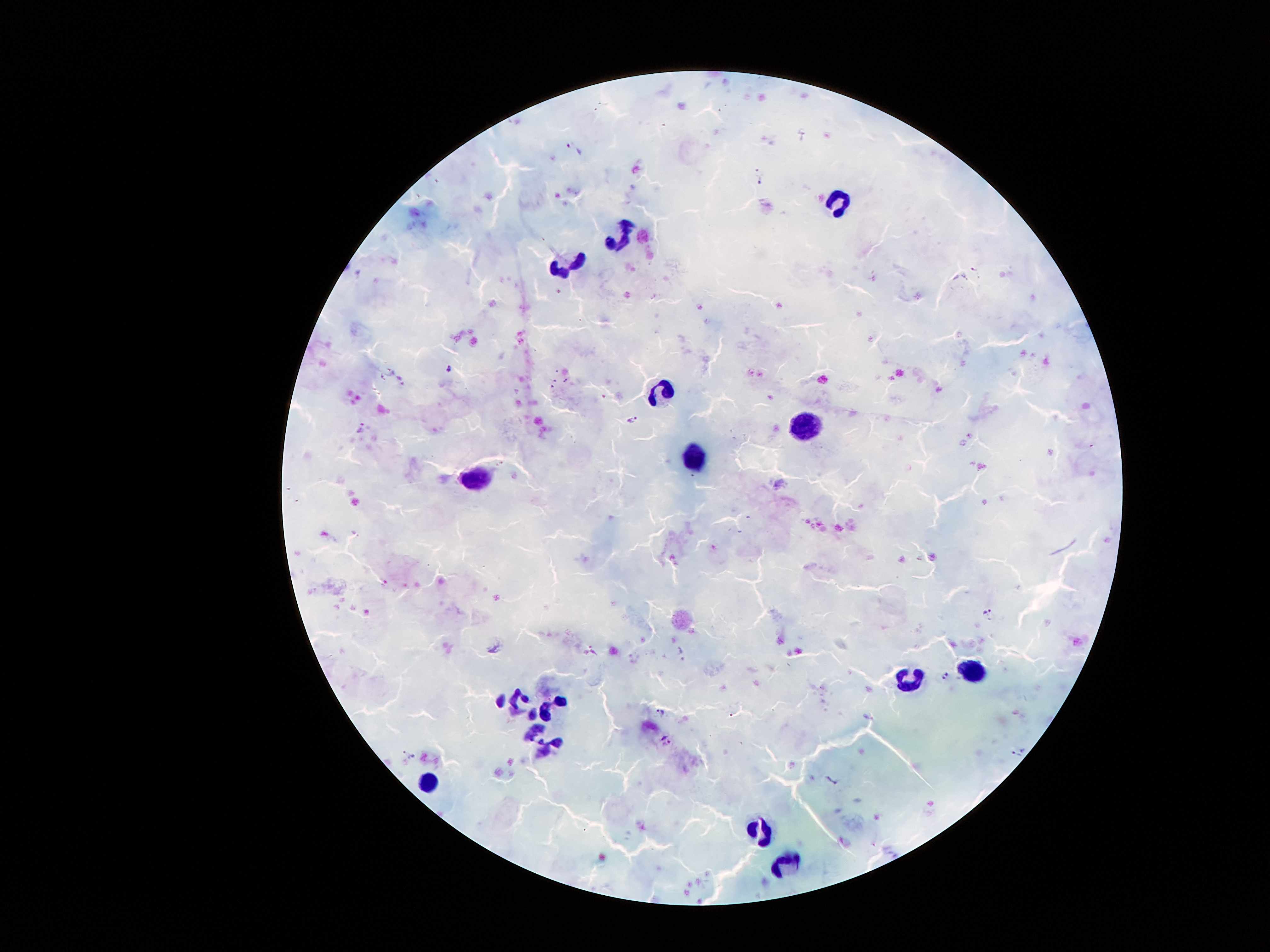

Approximate centers as [x, y] in pixels.
Summary:
  - Leukocyte locations: [835, 199], [619, 236], [561, 271], [664, 392], [808, 423], [696, 459], [471, 479], [976, 668], [909, 675], [515, 701], [548, 702], [541, 738], [423, 780], [761, 825], [790, 857]
  - Plasmodium parasite locations: [761, 181], [974, 270], [449, 369], [383, 377], [566, 381], [633, 420], [360, 427], [989, 613], [948, 678], [661, 712], [666, 741], [1015, 756]
  - Magnification: 100x
  - Preparation: thick blood smear
  - Image size: 1270×952 pixels
  - Capture: smartphone through the microscope eyepiece
  - Stain: Giemsa
  - Patient malaria status: infected with Plasmodium falciparum
  - Field of view: single